Report the malaria status of this cell.
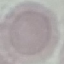
Uninfected.

Giemsa-stained preparation. Thin blood smear. Acquired by smartphone through the microscope eyepiece. Cell patch, automatically extracted from a larger field of view and resized to 64 × 64 pixels.